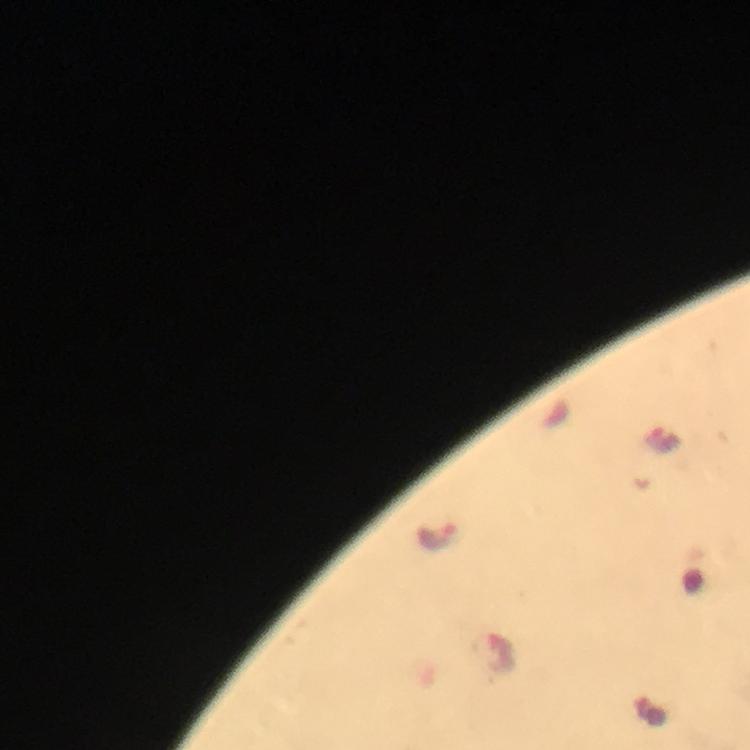

malaria parasite locations = approximate centers as (x, y) in pixels: (662, 440), (436, 536), (495, 654)
stain = Giemsa
cropped from = a single field of view
image size = 750×750 pixels
capture = smartphone camera through the microscope
preparation = thick blood smear
immersion oil = applied
context = from a malaria diagnostic workup
magnification = 100x